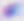
Micrograph. Toxoplasma gondii is shown. 400x magnification.